Report the malaria status of this cell.
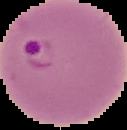

It is parasitized.

{
  "preparation": "thin blood smear",
  "image_type": "segmented cell region on a black background",
  "image_size": "127×130 pixels"
}